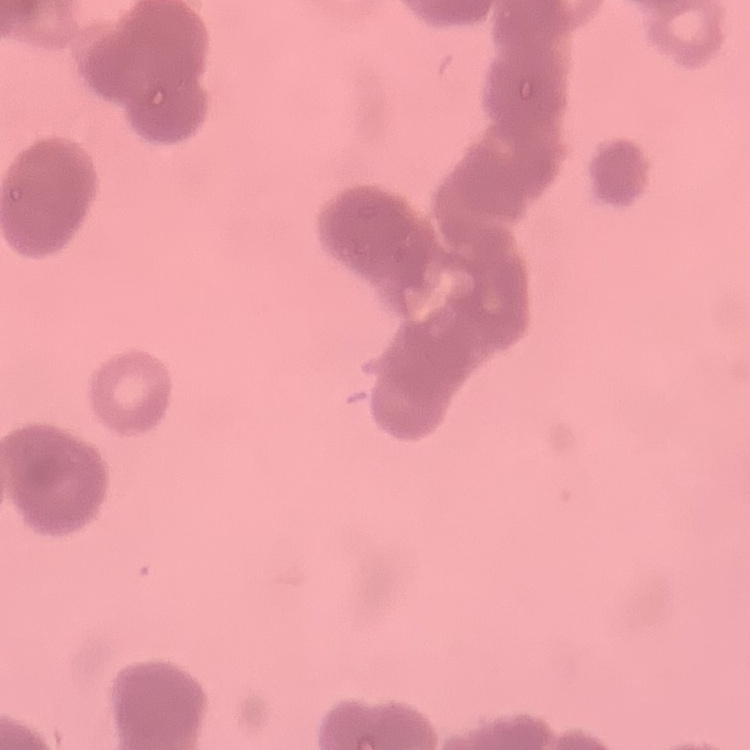

Summary:
  - Red blood cell morphology: rouleaux formation
  - Preparation: thin peripheral smear
  - Image type: one tile cut from a larger photomicrograph
  - Stain: Field's or Giemsa